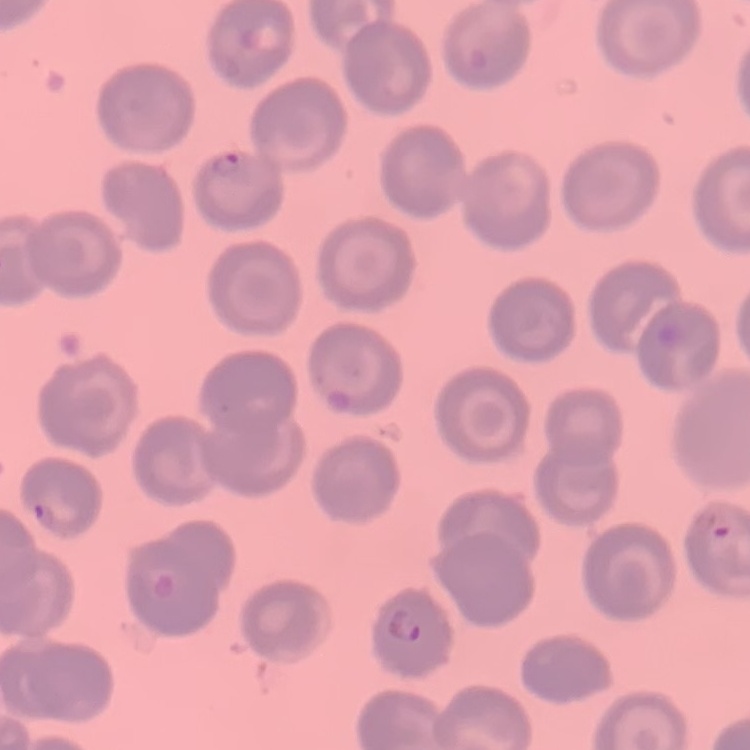
erythrocyte morphology = no rouleaux formation
image type = one tile cut from a larger photomicrograph
preparation = thin peripheral smear
stain = Field's or Giemsa